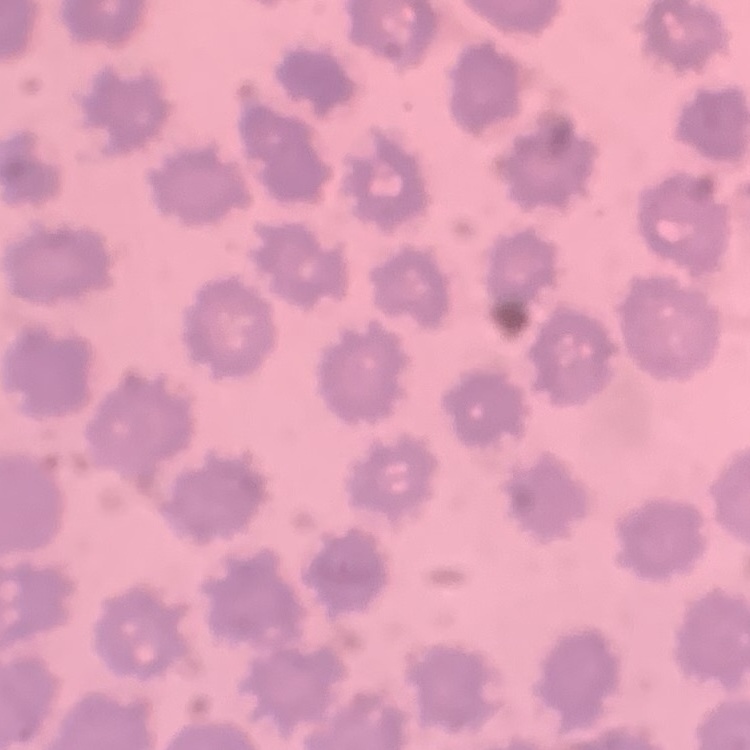
Summary:
  - Erythrocyte morphology: no rouleaux formation
  - Preparation: thin blood smear
  - Stain: Field's or Giemsa
  - Image type: one tile cut from a larger photomicrograph